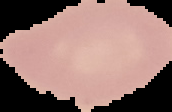
preparation = thin blood film
image type = segmented cell region with the area outside set to black
image size = 172×112 pixels
result = no Plasmodium parasites seen